Give the position of every Plasmodium parasite visible.
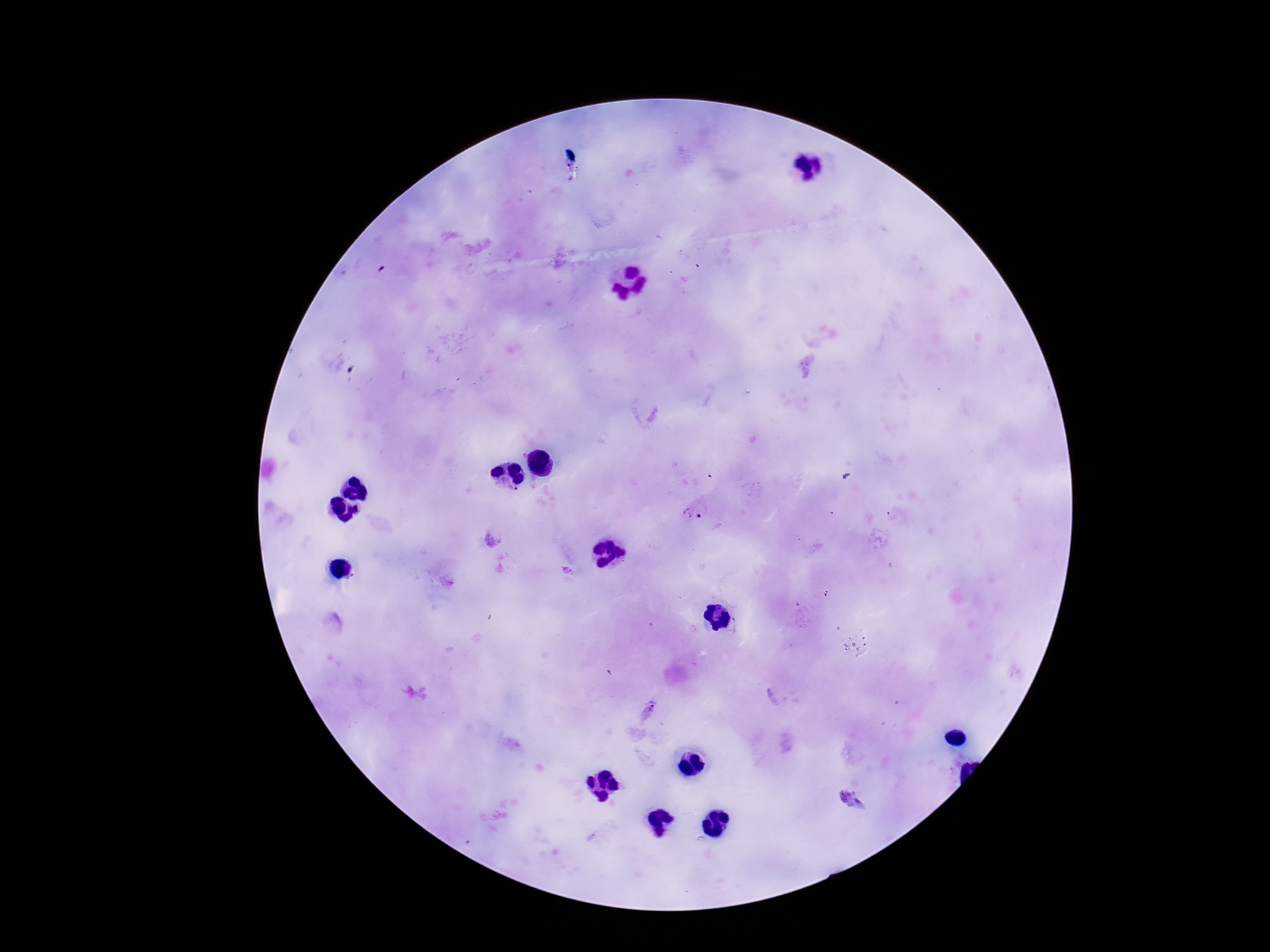

Approximate centers as {x, y} in pixels.
Plasmodium parasites: {694, 512}, {567, 571}, {649, 709}, {850, 800}.

Summary:
  - Image size: 1270×952 pixels
  - Stain: Giemsa
  - Capture: smartphone camera through the microscope eyepiece
  - Field of view: single
  - Patient malaria status: infected
  - Magnification: 100x
  - Preparation: thick blood smear